Point out each Plasmodium parasite.
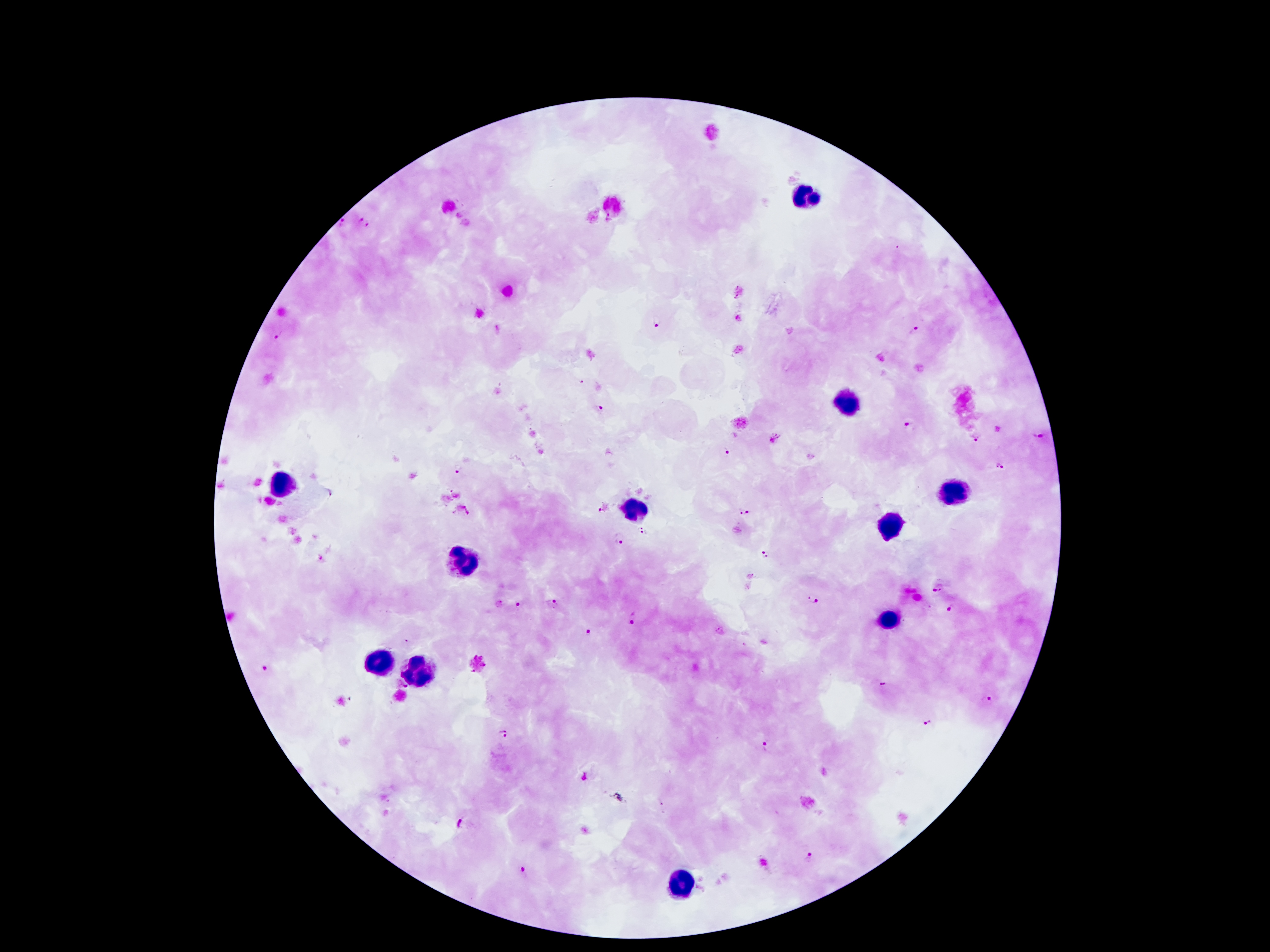
Approximate centers as {x, y} in pixels.
Plasmodium parasites: {657, 324}, {914, 330}, {278, 335}, {600, 407}, {911, 423}, {1037, 435}, {975, 437}, {725, 452}, {1002, 465}, {459, 470}, {603, 507}, {744, 513}, {641, 530}, {618, 537}, {764, 552}, {939, 588}, {815, 600}, {521, 603}, {552, 603}, {951, 609}, {635, 615}, {590, 630}, {263, 668}, {884, 684}, {986, 696}, {929, 723}, {504, 734}, {765, 746}, {462, 821}, {810, 858}, {522, 872}.

capture: smartphone through the microscope eyepiece
image_size: 1270×952 pixels
leukocyte_locations: 'approximate centers as {x, y} in pixels: {807, 194}, {849, 402}, {282, 483}, {951, 494}, {633, 509}, {888, 527}, {464, 557}, {885, 623}, {381, 663}, {422, 668}, {677, 881}'
stain: Giemsa
field_of_view: single
patient_malaria_status: infected with Plasmodium falciparum
preparation: thick peripheral-blood smear
magnification: 100x